Identify the preparation type.
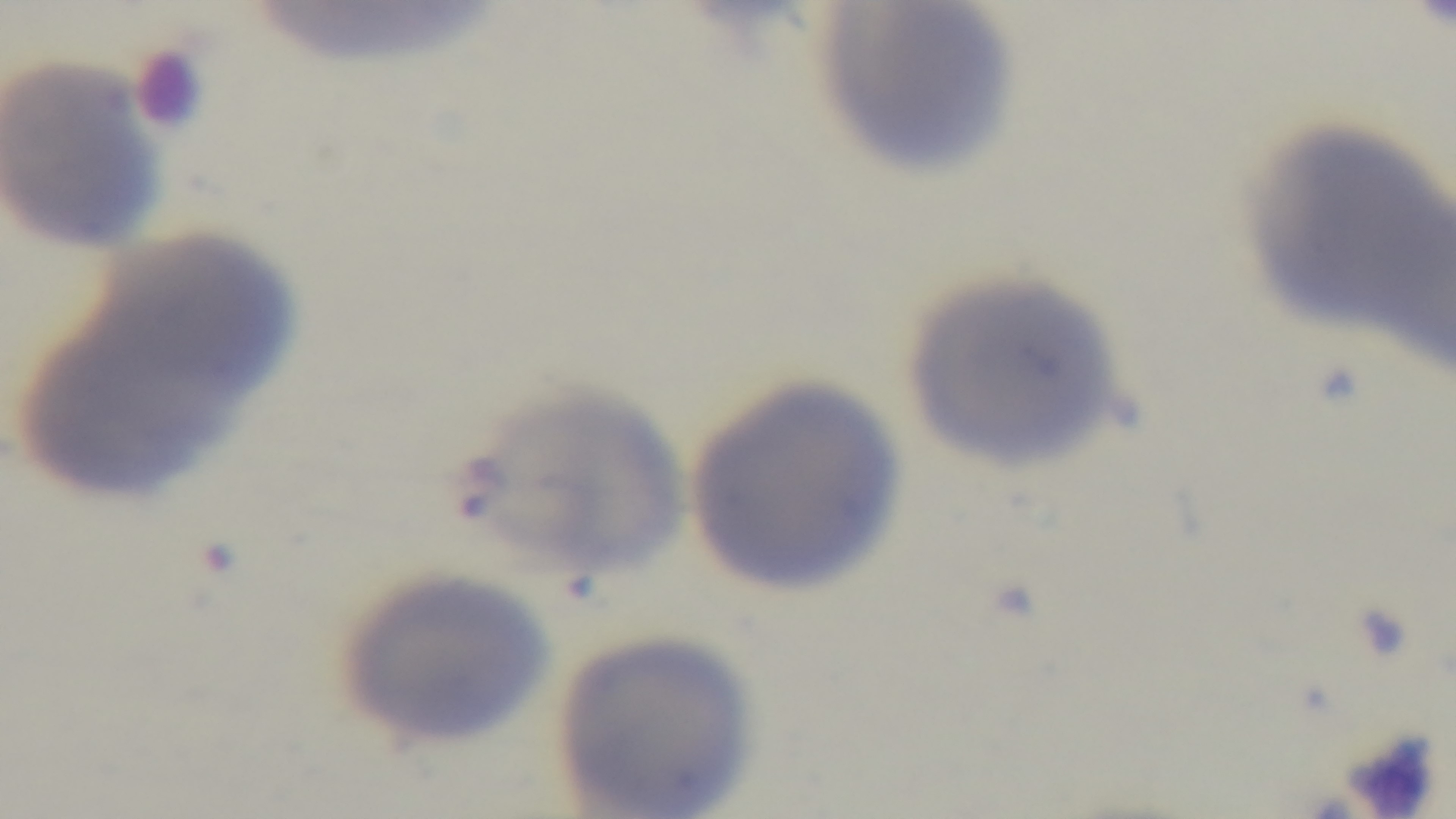
It is a thin blood film.

Malaria status: uninfected. Light microscopy. Giemsa-stained. 100x oil-immersion objective. Mounted 4K digital camera. Single field of view.